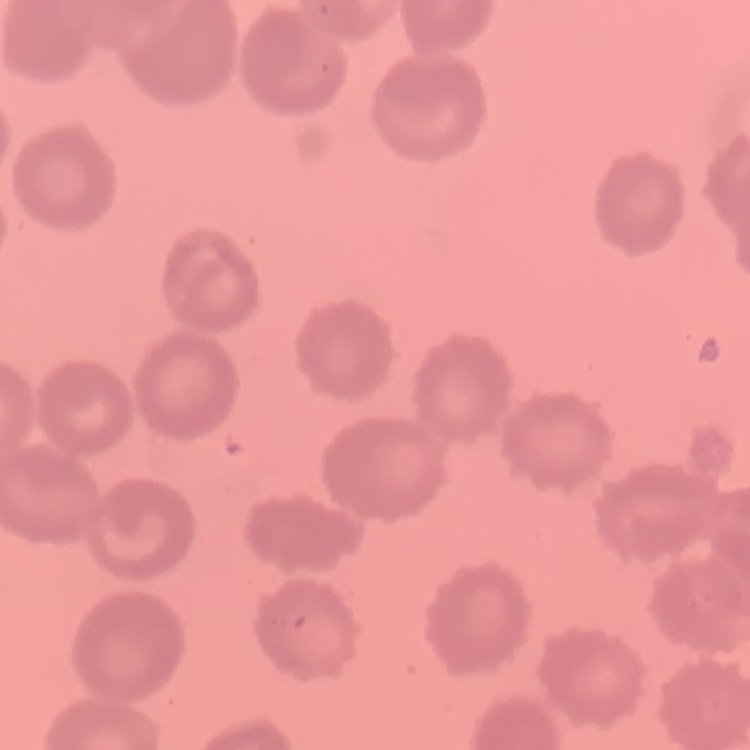

erythrocyte morphology = no rouleaux formation
image type = one tile cut from a larger photomicrograph
preparation = thin blood film
stain = Field's or Giemsa